Locate every Plasmodium parasite.
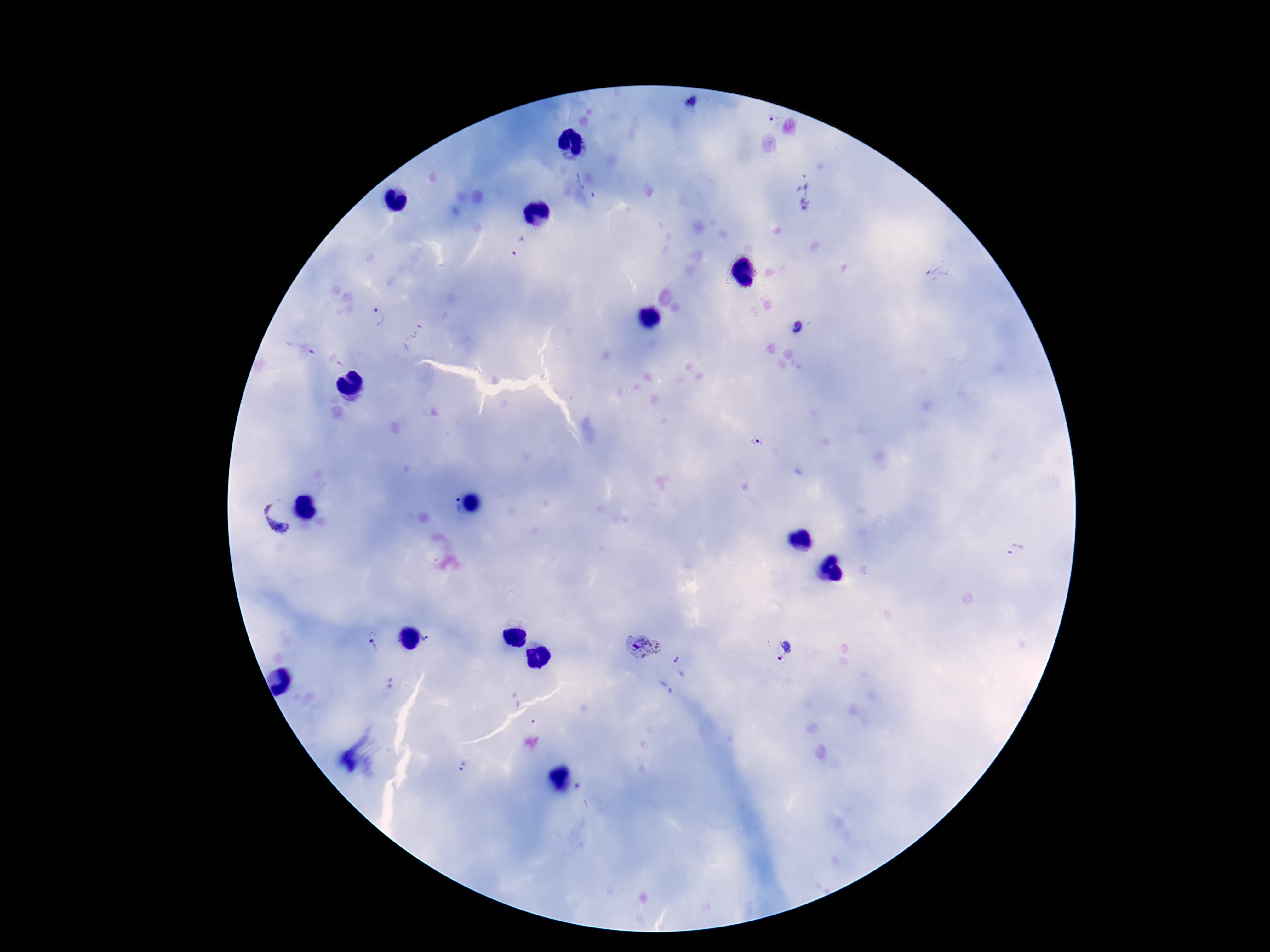
Approximate centers as [x, y] in pixels.
Plasmodium parasites: [693, 101], [589, 186], [806, 194], [519, 246], [937, 275], [378, 316], [798, 330], [412, 335], [305, 349], [757, 441], [452, 508], [277, 519], [1016, 550], [432, 637], [374, 641], [642, 646], [784, 650], [682, 664], [391, 683], [663, 688], [462, 767], [580, 787].

Image is 1270×952 pixels. Patient malaria status: positive. 100x magnification. Thick peripheral-blood smear. Giemsa stain. Photographed through the microscope eyepiece with a smartphone camera. One field from this slide.